Assess this cell for malaria.
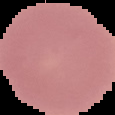

It is uninfected.

image_type: cell region segmented out of the field of view; surrounding area masked to black
preparation: thin blood smear
image_size: 115×115 pixels